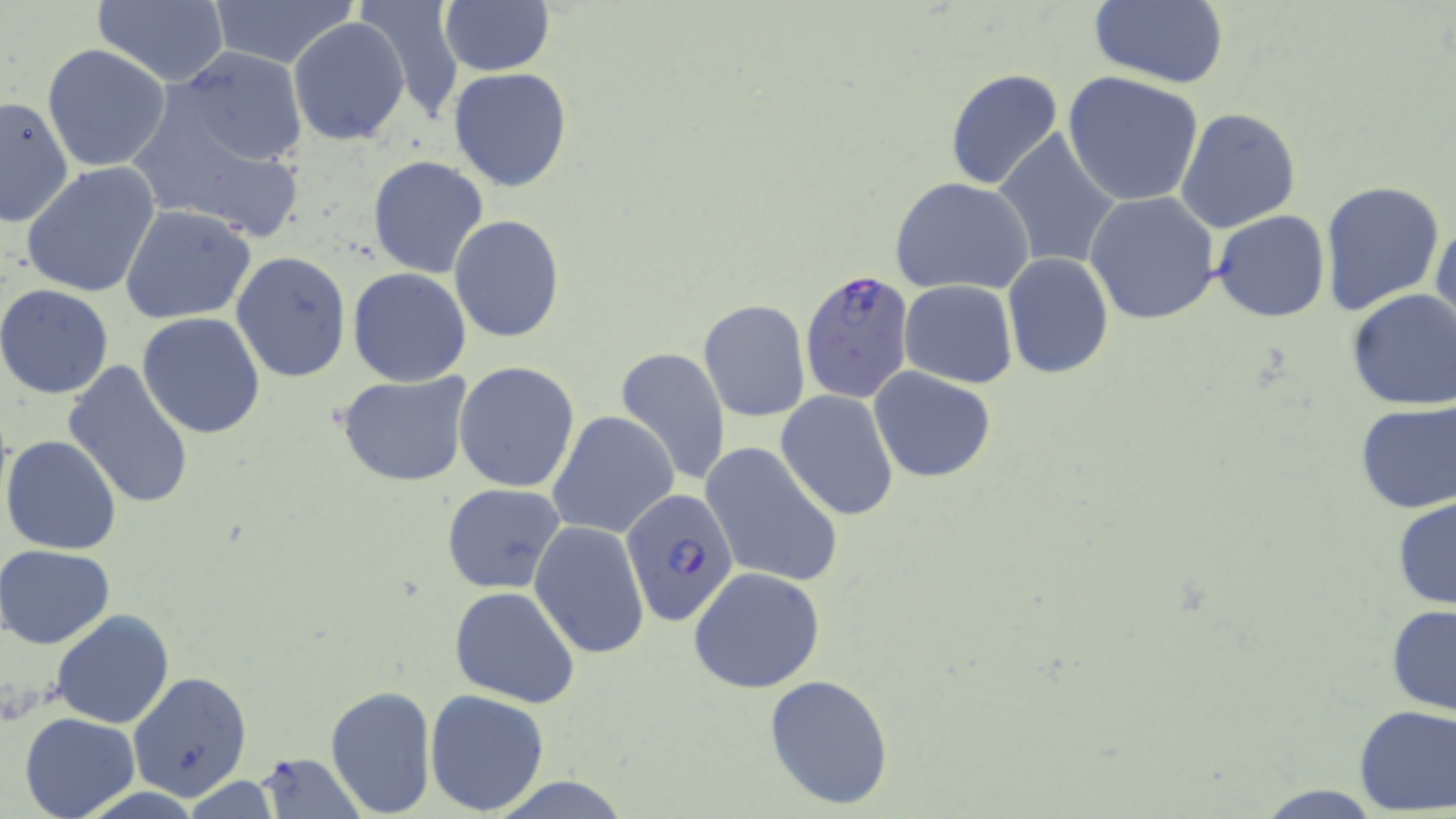
slide_level_diagnosis: Plasmodium falciparum
image_size: 1456×819 pixels
magnification: 1000x
field_of_view: single
uninfected_red_blood_cell_locations: 'approximate bounding boxes as (x1,y1)-(x2,y2) corner pairs in pixels: (208,0)-(359,69), (352,0)-(468,126), (1086,0)-(1229,88), (91,1)-(230,85), (440,2)-(555,76), (288,17)-(411,146), (41,43)-(172,175), (165,49)-(310,170), (448,67)-(573,193), (945,68)-(1065,192), (1062,73)-(1206,208), (125,87)-(310,244), (0,95)-(74,229), (1174,107)-(1302,233), (992,129)-(1122,272), (367,155)-(488,278), (20,161)-(161,298), (890,176)-(1036,295), (1318,179)-(1446,317), (1084,192)-(1221,324), (120,203)-(257,324), (1212,211)-(1330,323), (1431,212)-(1455,343), (449,214)-(565,342), (230,251)-(352,382), (1001,253)-(1114,379), (347,268)-(471,386), (898,281)-(1018,386), (0,284)-(114,399), (1344,289)-(1456,411), (698,299)-(810,423), (137,311)-(265,438), (613,347)-(729,488), (62,360)-(196,511), (454,361)-(580,491), (869,368)-(996,484), (336,371)-(475,489), (776,390)-(898,522), (1354,400)-(1456,514), (548,410)-(679,541), (1,435)-(123,555), (700,442)-(844,589), (441,483)-(566,594), (1392,496)-(1456,612), (530,519)-(651,662), (1,544)-(117,649), (688,566)-(826,694), (449,586)-(581,709), (1386,603)-(1456,715), (50,610)-(176,729), (127,671)-(254,800), (763,673)-(895,809), (324,683)-(437,817), (424,689)-(549,814), (1352,704)-(1456,816), (19,710)-(140,818), (256,752)-(364,818), (178,777)-(285,816), (1250,785)-(1391,816)'
stain: May-Grünwald-Giemsa
preparation: thin blood smear
modality: light microscopy
plasmodium_falciparum_infected_red_blood_cell_locations: 'approximate bounding boxes as (x1,y1)-(x2,y2) corner pairs in pixels: (799,268)-(917,402), (622,490)-(743,632)'